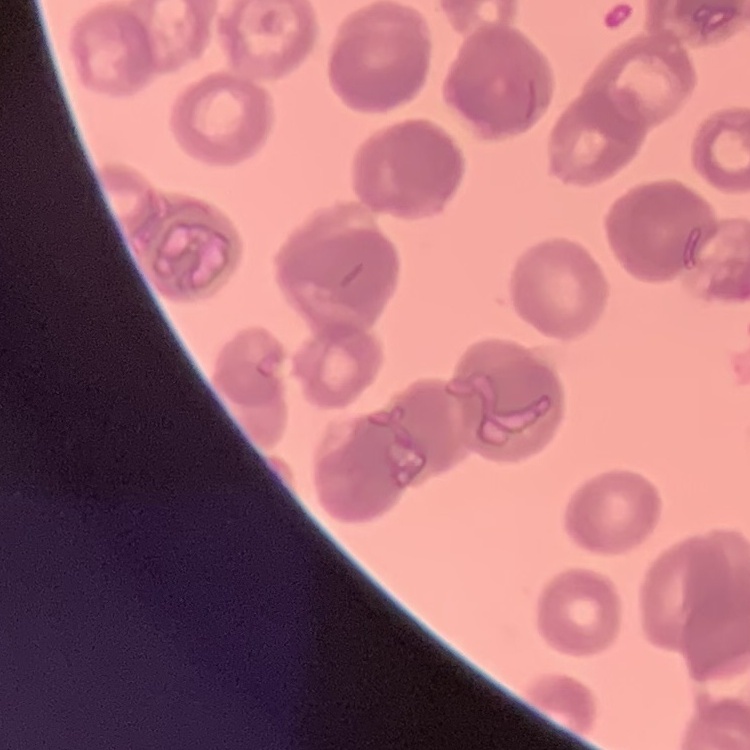
Summary:
  - Erythrocyte morphology: rouleaux formation
  - Preparation: thin blood smear
  - Image type: one tile cut from a larger photomicrograph
  - Stain: Field's or Giemsa